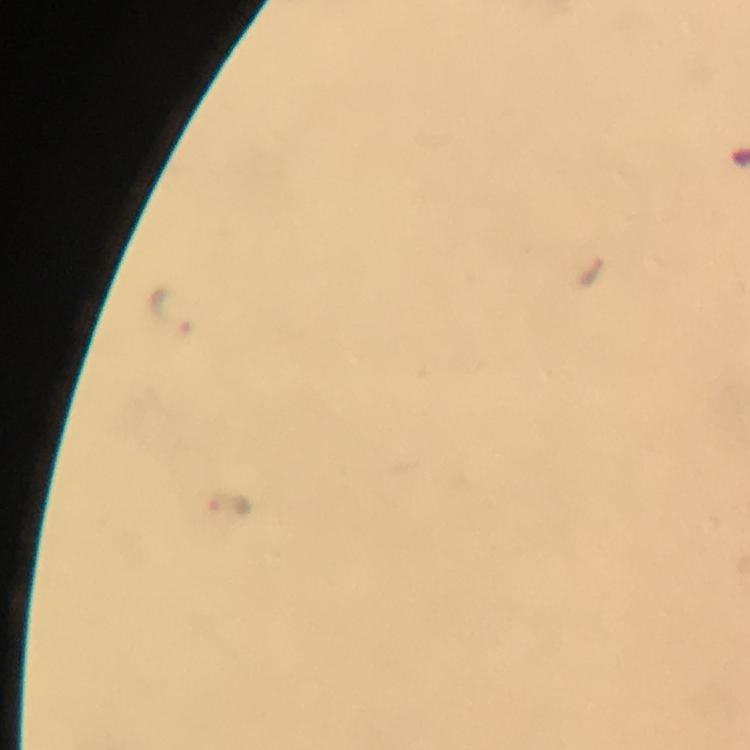

cropped_from: one field of view
image_size: 750×750 pixels
immersion_oil: applied
preparation: thick smear
stain: Giemsa
magnification: 100x
capture: smartphone camera through the microscope
malaria_parasite_locations: 'approximate centers as [x, y] in pixels: [172, 315], [228, 502]'
context: from a malaria diagnostic workup